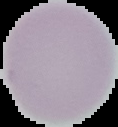
result: no Plasmodium parasites detected
image_size: 118×127 pixels
image_type: cell region segmented out of the field of view; surrounding area masked to black
preparation: thin blood film